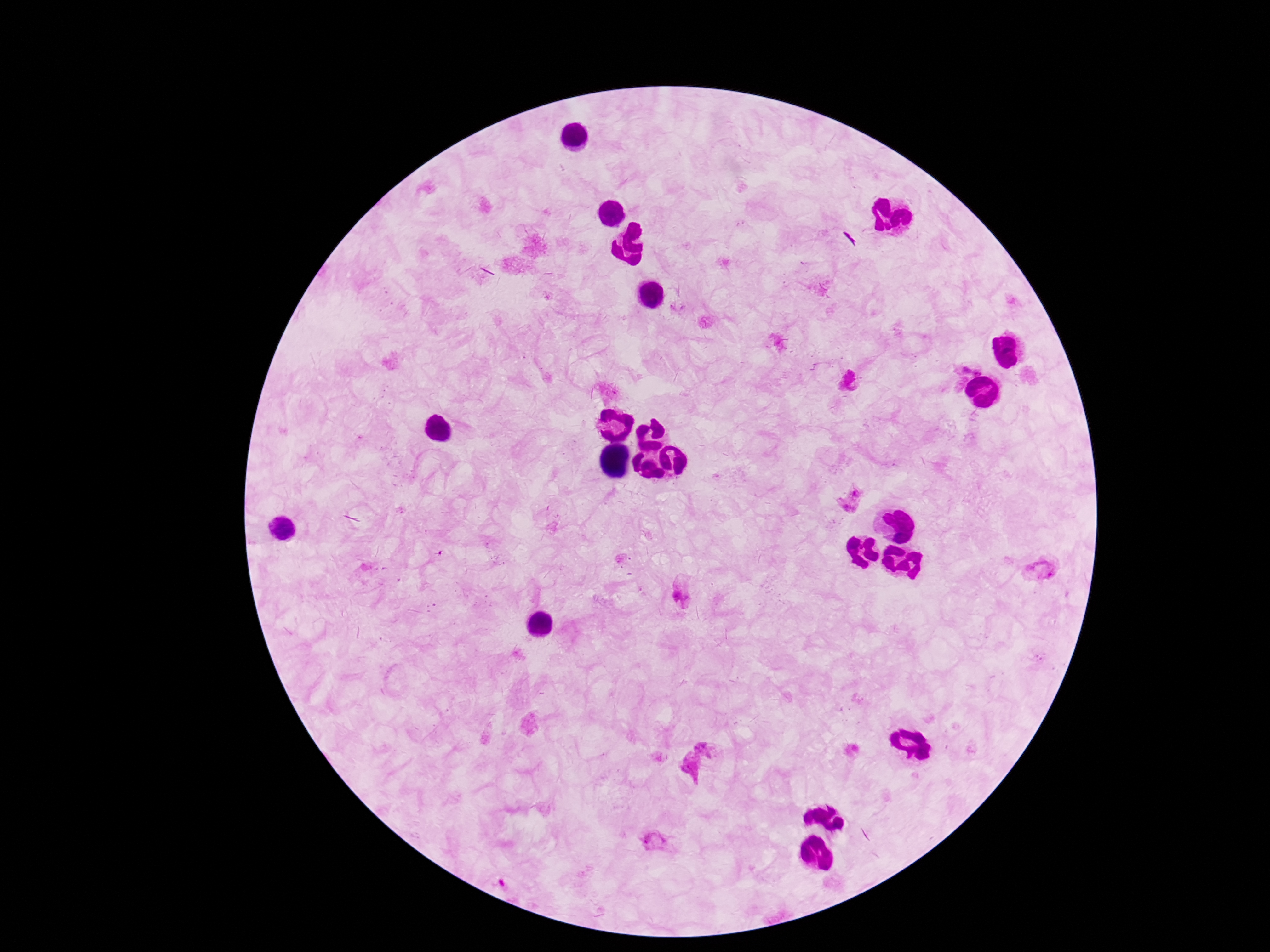
Approximate centers as (x, y) in pixels.
Summary:
  - Plasmodium parasite locations: (965, 370), (977, 373), (960, 382), (855, 492), (846, 507), (1040, 571), (683, 593), (705, 746), (691, 767), (654, 841), (503, 882)
  - Patient malaria status: positive
  - Magnification: 100x
  - Field of view: one from this slide
  - Capture: smartphone camera through the microscope eyepiece
  - Stain: Giemsa
  - Preparation: thick blood smear
  - Image size: 1270×952 pixels